Point out every malaria parasite.
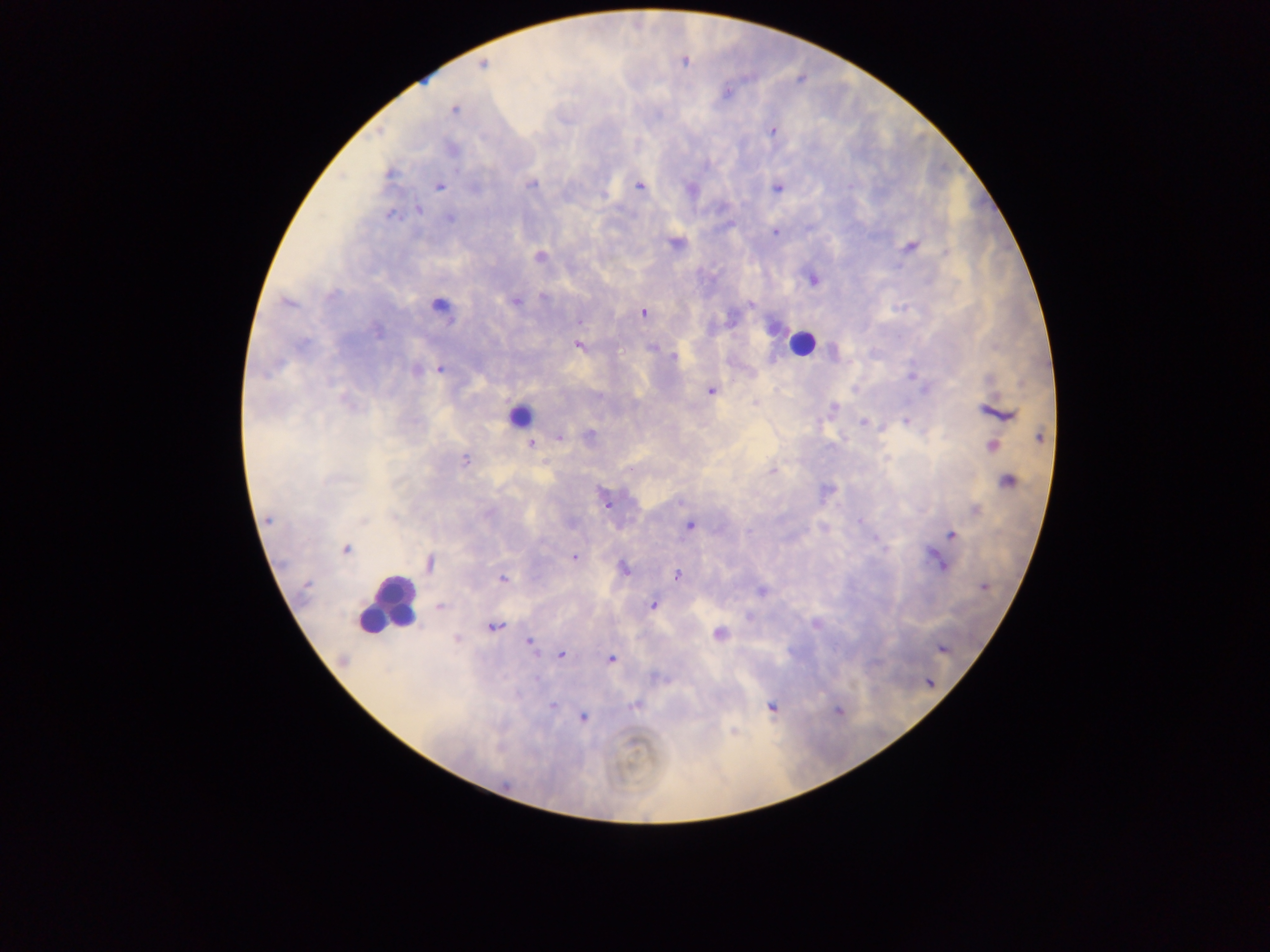
Approximate centers as {x, y} in pixels.
Malaria parasites: {684, 62}, {482, 64}, {727, 91}, {454, 110}, {772, 130}, {452, 149}, {390, 173}, {532, 184}, {439, 186}, {639, 186}, {776, 188}, {418, 209}, {389, 215}, {449, 219}, {774, 232}, {674, 243}, {911, 246}, {946, 252}, {540, 256}, {813, 279}, {330, 295}, {544, 297}, {516, 301}, {287, 303}, {750, 304}, {643, 312}, {729, 321}, {377, 331}, {303, 343}, {579, 345}, {653, 348}, {673, 356}, {440, 369}, {416, 370}, {911, 378}, {710, 391}, {834, 406}, {995, 413}, {863, 422}, {906, 422}, {590, 434}, {559, 437}, {1040, 437}, {530, 444}, {992, 447}, {465, 460}, {631, 469}, {772, 470}, {1007, 480}, {679, 502}, {607, 505}, {975, 510}, {268, 519}, {860, 521}, {363, 522}, {690, 526}, {952, 535}, {346, 548}, {574, 558}, {430, 564}, {940, 564}, {625, 568}, {677, 574}, {503, 578}, {985, 587}, {762, 591}, {653, 605}, {441, 607}, {494, 626}, {718, 634}, {457, 639}, {529, 642}, {942, 649}, {562, 655}, {342, 659}, {610, 659}, {537, 678}, {552, 706}, {633, 706}, {772, 707}, {837, 711}, {584, 718}.

capture = mobile-phone photograph through a microscope
field of view = single
country = Ghana
preparation = thick blood smear
leukocyte locations = approximate centers as {x, y} in pixels: {439, 305}, {802, 343}, {518, 417}, {387, 605}
image size = 1270×952 pixels